Classify this cell by malaria status.
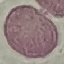

It is uninfected.

Giemsa stain. Cell patch, automatically extracted from a larger field of view and resized to 64 × 64 pixels. Thin blood film. Photographed with a smartphone camera at the microscope eyepiece.